Outline each Plasmodium malariae-infected red blood cell.
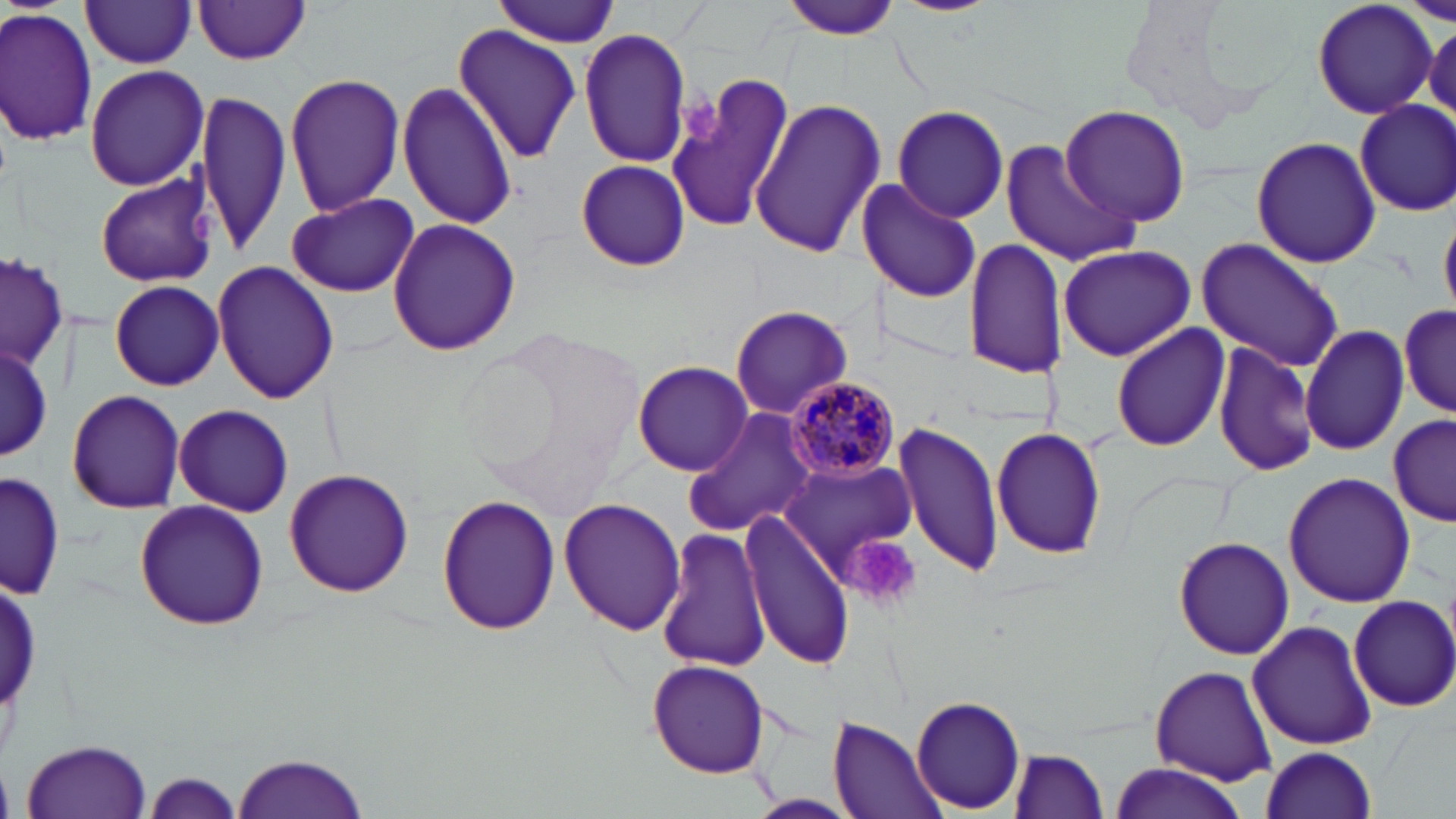

Approximate bounding boxes as named x1/y1/x2/y2 corners in pixels.
Plasmodium malariae-infected red blood cells: (x1=786, y1=376, x2=902, y2=483).

Platelet locations: (x1=678, y1=87, x2=723, y2=146), (x1=186, y1=210, x2=218, y2=244), (x1=843, y1=533, x2=922, y2=609). Uninfected red blood cell locations: (x1=492, y1=0, x2=624, y2=45), (x1=1312, y1=0, x2=1437, y2=121), (x1=1404, y1=0, x2=1453, y2=26), (x1=779, y1=1, x2=907, y2=39), (x1=80, y1=2, x2=198, y2=69), (x1=195, y1=2, x2=311, y2=66), (x1=0, y1=7, x2=100, y2=144), (x1=1422, y1=18, x2=1456, y2=125), (x1=451, y1=25, x2=584, y2=163), (x1=578, y1=26, x2=692, y2=168), (x1=83, y1=64, x2=210, y2=191), (x1=664, y1=71, x2=800, y2=233), (x1=283, y1=73, x2=406, y2=217), (x1=397, y1=81, x2=518, y2=232), (x1=196, y1=89, x2=291, y2=255), (x1=749, y1=98, x2=884, y2=259), (x1=1354, y1=99, x2=1456, y2=217), (x1=1059, y1=104, x2=1192, y2=228), (x1=892, y1=105, x2=1010, y2=221), (x1=1251, y1=135, x2=1382, y2=268), (x1=1002, y1=140, x2=1135, y2=266), (x1=574, y1=159, x2=691, y2=271), (x1=94, y1=172, x2=218, y2=288), (x1=861, y1=176, x2=983, y2=305), (x1=283, y1=191, x2=421, y2=297), (x1=386, y1=216, x2=521, y2=357), (x1=962, y1=237, x2=1062, y2=380), (x1=1195, y1=238, x2=1345, y2=372), (x1=1056, y1=245, x2=1197, y2=361), (x1=1, y1=252, x2=67, y2=372), (x1=212, y1=260, x2=340, y2=405), (x1=109, y1=280, x2=225, y2=390), (x1=1398, y1=298, x2=1454, y2=420), (x1=730, y1=304, x2=852, y2=419), (x1=1110, y1=320, x2=1230, y2=452), (x1=1301, y1=323, x2=1411, y2=456), (x1=1213, y1=340, x2=1319, y2=479), (x1=1, y1=343, x2=52, y2=458), (x1=631, y1=360, x2=754, y2=476), (x1=66, y1=389, x2=186, y2=514), (x1=172, y1=403, x2=294, y2=517), (x1=684, y1=407, x2=817, y2=535), (x1=1388, y1=415, x2=1454, y2=529), (x1=894, y1=420, x2=1005, y2=579), (x1=991, y1=425, x2=1109, y2=561), (x1=782, y1=459, x2=917, y2=578), (x1=281, y1=465, x2=414, y2=597), (x1=1284, y1=471, x2=1417, y2=609), (x1=1, y1=472, x2=63, y2=600), (x1=436, y1=495, x2=560, y2=636), (x1=559, y1=497, x2=686, y2=635), (x1=133, y1=499, x2=269, y2=632), (x1=742, y1=510, x2=855, y2=671), (x1=658, y1=530, x2=771, y2=676), (x1=1172, y1=535, x2=1294, y2=661), (x1=1347, y1=594, x2=1456, y2=714), (x1=1247, y1=619, x2=1378, y2=752), (x1=647, y1=660, x2=771, y2=777), (x1=1149, y1=664, x2=1278, y2=788), (x1=911, y1=694, x2=1026, y2=813), (x1=830, y1=716, x2=949, y2=819), (x1=20, y1=739, x2=156, y2=818), (x1=1259, y1=747, x2=1377, y2=818), (x1=1008, y1=748, x2=1112, y2=819), (x1=232, y1=750, x2=370, y2=818), (x1=1106, y1=763, x2=1250, y2=817), (x1=141, y1=771, x2=248, y2=818), (x1=747, y1=795, x2=853, y2=818). Slide-level diagnosis: Plasmodium malariae. 1000x magnification. Image is 1456×819 pixels. Light microscopy. Single field of view. Thin blood smear. May-Grünwald-Giemsa stain.